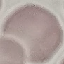
Malaria status: uninfected. Thin blood smear. Acquired by smartphone through the microscope eyepiece. Cell patch, automatically extracted from a larger field of view and resized to 64 × 64 pixels. Giemsa stain.